Identify the parasite.
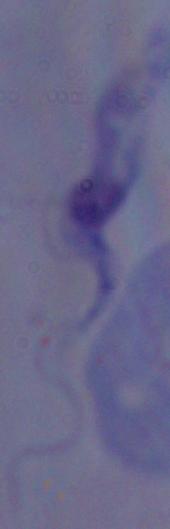

This is a trypanosome.

{
  "magnification": "1000x",
  "modality": "micrograph"
}